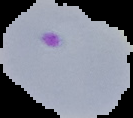
Malaria status: parasitized. Image is 133×118 pixels. The area outside the segmented cell region is set to black. From a thin blood smear.